Give the position of every Plasmodium parasite visible.
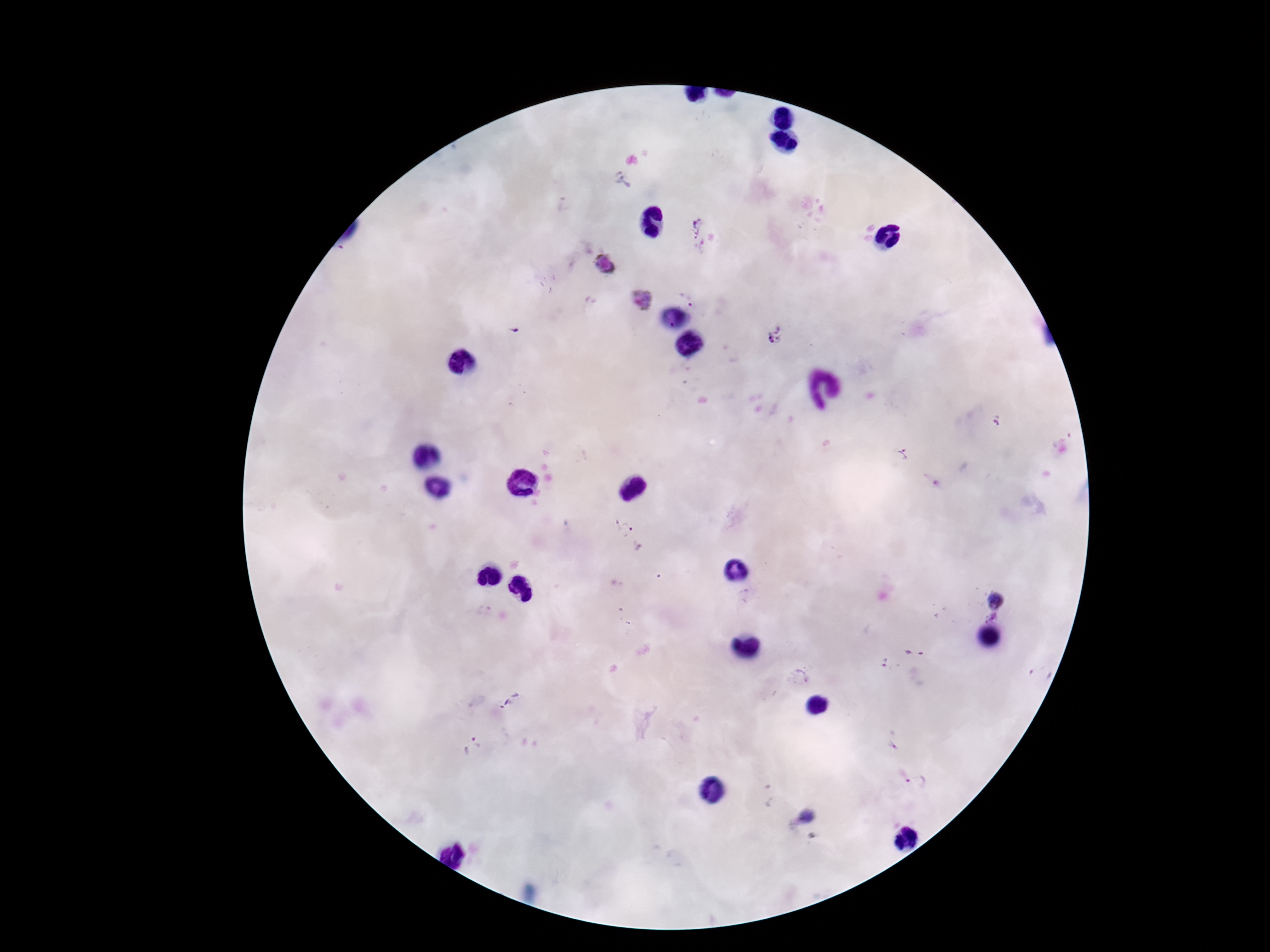

Approximate centers as (x, y) in pixels.
Plasmodium parasites: (621, 179), (565, 205), (695, 224), (604, 263), (688, 297), (642, 301), (514, 332), (776, 336), (998, 421), (904, 455), (622, 525), (996, 600), (485, 611), (992, 617), (913, 652), (880, 662), (1040, 675), (801, 679), (893, 739), (473, 746), (916, 782), (767, 797), (807, 817).

Image is 1270×952 pixels. Photographed through the microscope eyepiece with a smartphone camera. Giemsa-stained preparation. Thick blood film. Patient malaria status: positive. Single field of view. 100x magnification.